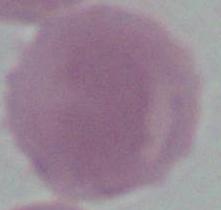

Summary:
  - Modality: micrograph
  - Identification: red blood cell
  - Magnification: 1000x